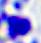

{
  "identification": "leukocyte",
  "magnification": "400x",
  "modality": "micrograph"
}